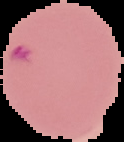
Malaria status: parasitized. The area outside the segmented cell region is set to black. From a thin blood film. Image is 124×142 pixels.